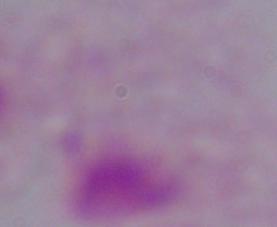

modality: micrograph
identification: trichomonad
magnification: 1000x